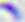
Toxoplasma gondii is seen. Photomicrograph. 400x magnification.